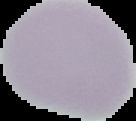

image type = segmented cell region with the area outside set to black
image size = 136×121 pixels
malaria status = uninfected
preparation = thin blood film